Locate every blood parasite and identify its species.
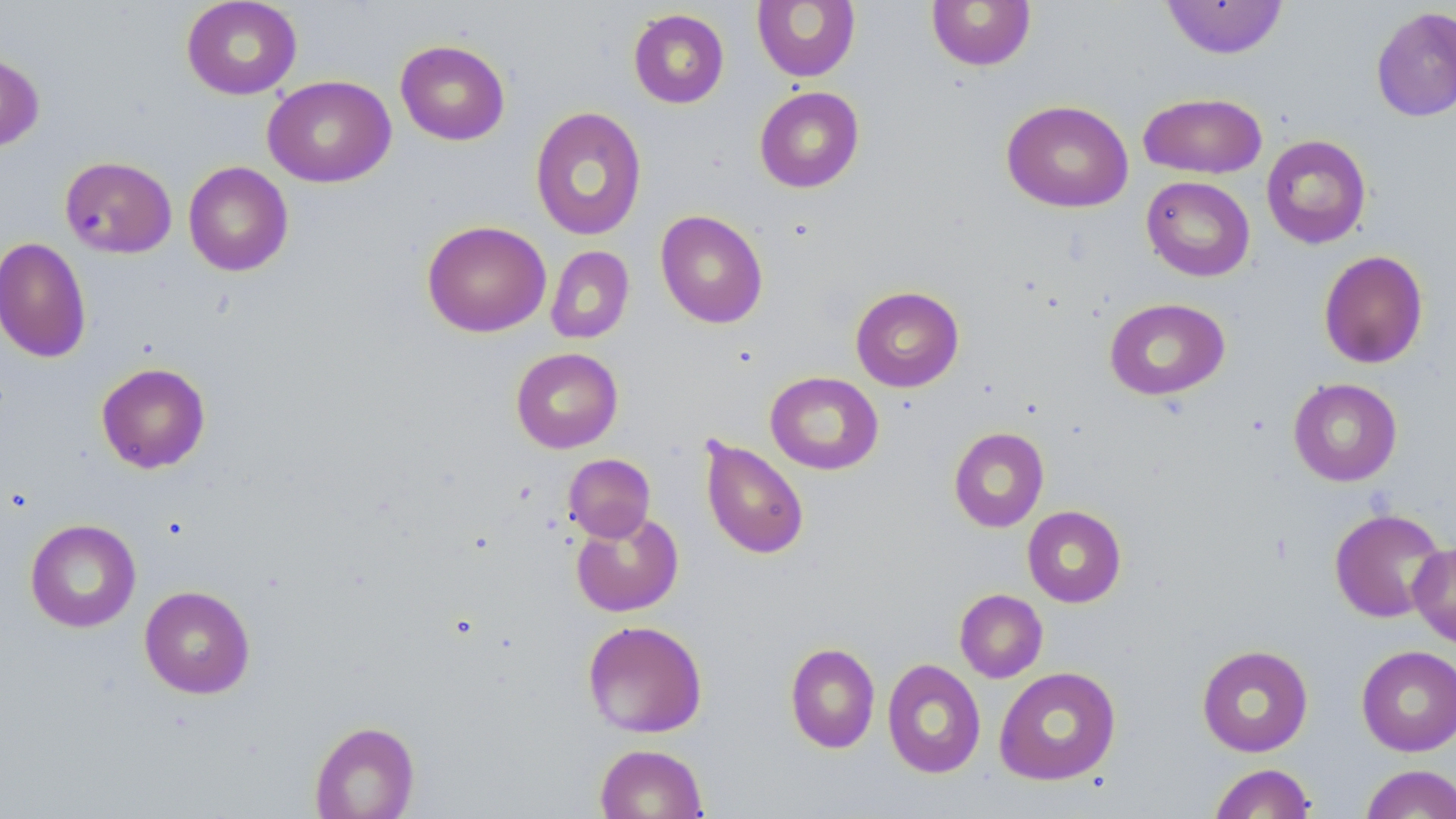

No blood parasites seen.

Approximate bounding boxes as (x1,y1)-(x2,y2) corner pairs in pixels. Uninfected red blood cell locations: (181,0)-(302,100), (752,0)-(860,82), (926,0)-(1036,71), (1161,1)-(1289,59), (1370,5)-(1456,123), (628,8)-(729,108), (395,39)-(510,145), (0,52)-(45,151), (263,75)-(396,188), (754,86)-(865,193), (1138,92)-(1266,179), (1001,100)-(1134,213), (530,106)-(647,241), (1261,134)-(1372,249), (60,156)-(177,259), (183,161)-(293,276), (1141,176)-(1255,281), (655,209)-(768,328), (421,220)-(551,337), (0,237)-(92,363), (546,246)-(635,343), (1318,250)-(1429,369), (850,286)-(964,392), (1104,298)-(1230,400), (511,347)-(623,453), (96,362)-(210,473), (765,371)-(884,475), (1289,378)-(1403,487), (949,427)-(1049,532), (699,436)-(809,560), (563,453)-(655,541), (1022,505)-(1126,607), (1329,507)-(1448,623), (571,510)-(684,617), (25,518)-(141,633), (1409,541)-(1456,648), (139,585)-(255,698), (954,589)-(1048,683), (582,619)-(708,738), (785,642)-(880,754), (1196,644)-(1314,757), (1356,645)-(1456,756), (882,659)-(986,778), (994,666)-(1121,785), (309,721)-(420,818), (594,743)-(707,818), (1208,762)-(1317,818), (1360,764)-(1456,819). Slide-level diagnosis: no evidence of blood parasites. Optical microscopy. One field of a larger specimen. May-Grünwald-Giemsa-stained preparation. Thin blood smear. Image is 1456×819 pixels. Captured at 1000x magnification.